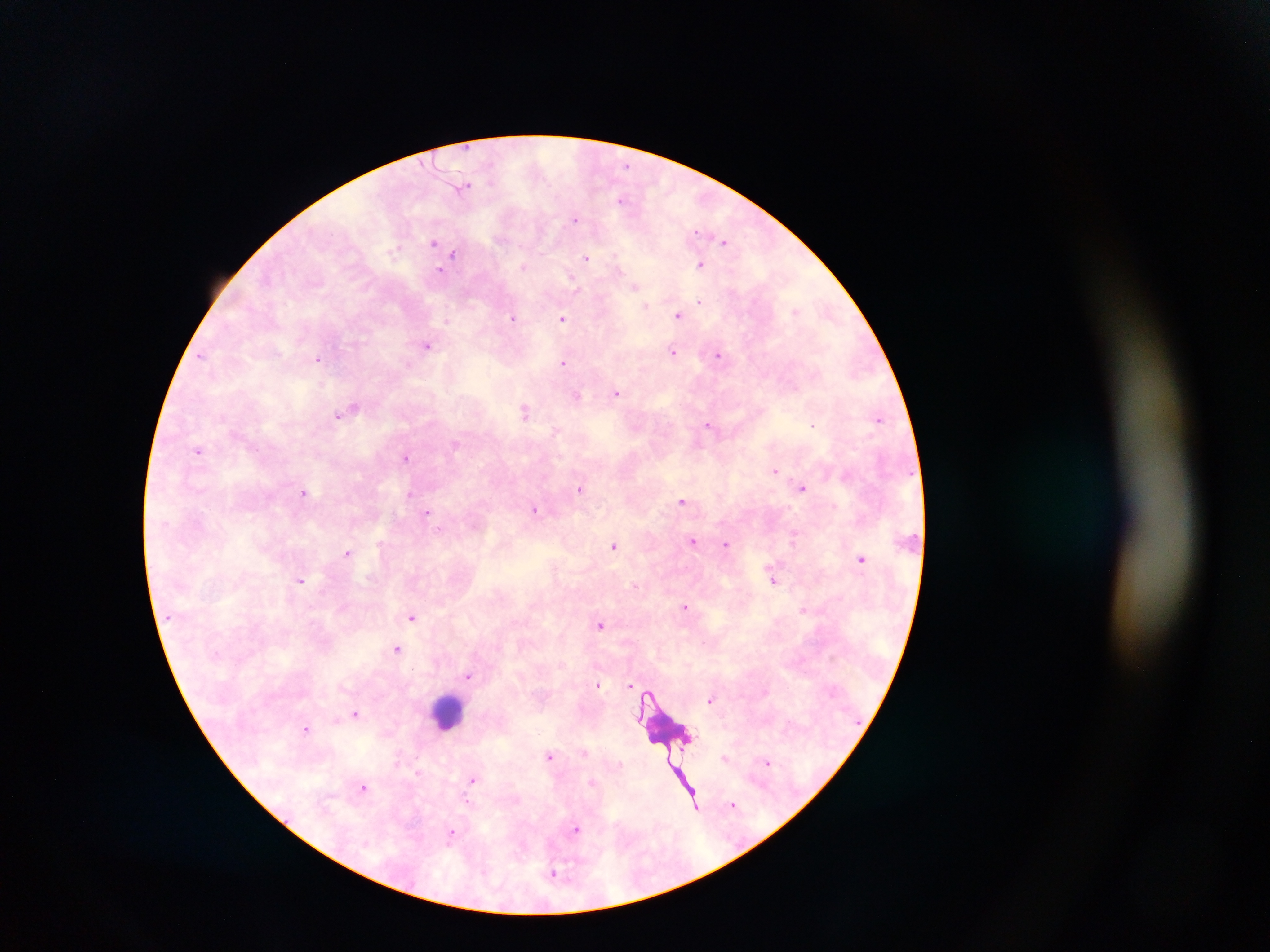
capture = mobile-phone photograph through a microscope
leukocyte locations = approximate centers as (x, y) in pixels: (453, 709)
preparation = thick blood smear
field of view = single
country = Ghana
malaria parasite locations = approximate centers as (x, y) in pixels: (468, 185), (623, 199), (576, 219), (433, 242), (722, 242), (455, 255), (586, 258), (701, 265), (699, 302), (646, 306), (796, 310), (679, 314), (513, 319), (446, 320), (563, 320), (426, 346), (672, 353), (719, 354), (318, 360), (563, 361), (796, 387), (615, 394), (525, 413), (337, 416), (709, 424), (815, 424), (198, 450), (406, 457), (774, 471), (581, 487), (803, 489), (410, 493), (305, 495), (683, 502), (535, 510), (427, 512), (795, 538), (694, 542), (727, 544), (613, 546), (348, 551), (862, 560), (301, 580), (685, 607), (803, 610), (410, 619), (600, 626), (396, 649), (468, 675), (631, 685), (598, 686), (649, 692), (709, 701), (356, 715), (336, 719), (307, 730), (585, 752), (549, 755), (767, 763), (471, 781), (593, 782), (364, 786), (464, 800), (695, 803), (734, 803), (577, 830), (452, 831)
image size = 1270×952 pixels